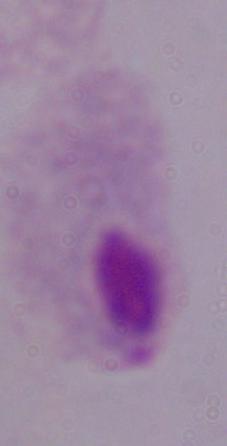
Summary:
  - Magnification: 1000x
  - Modality: photomicrograph
  - Identification: trichomonad